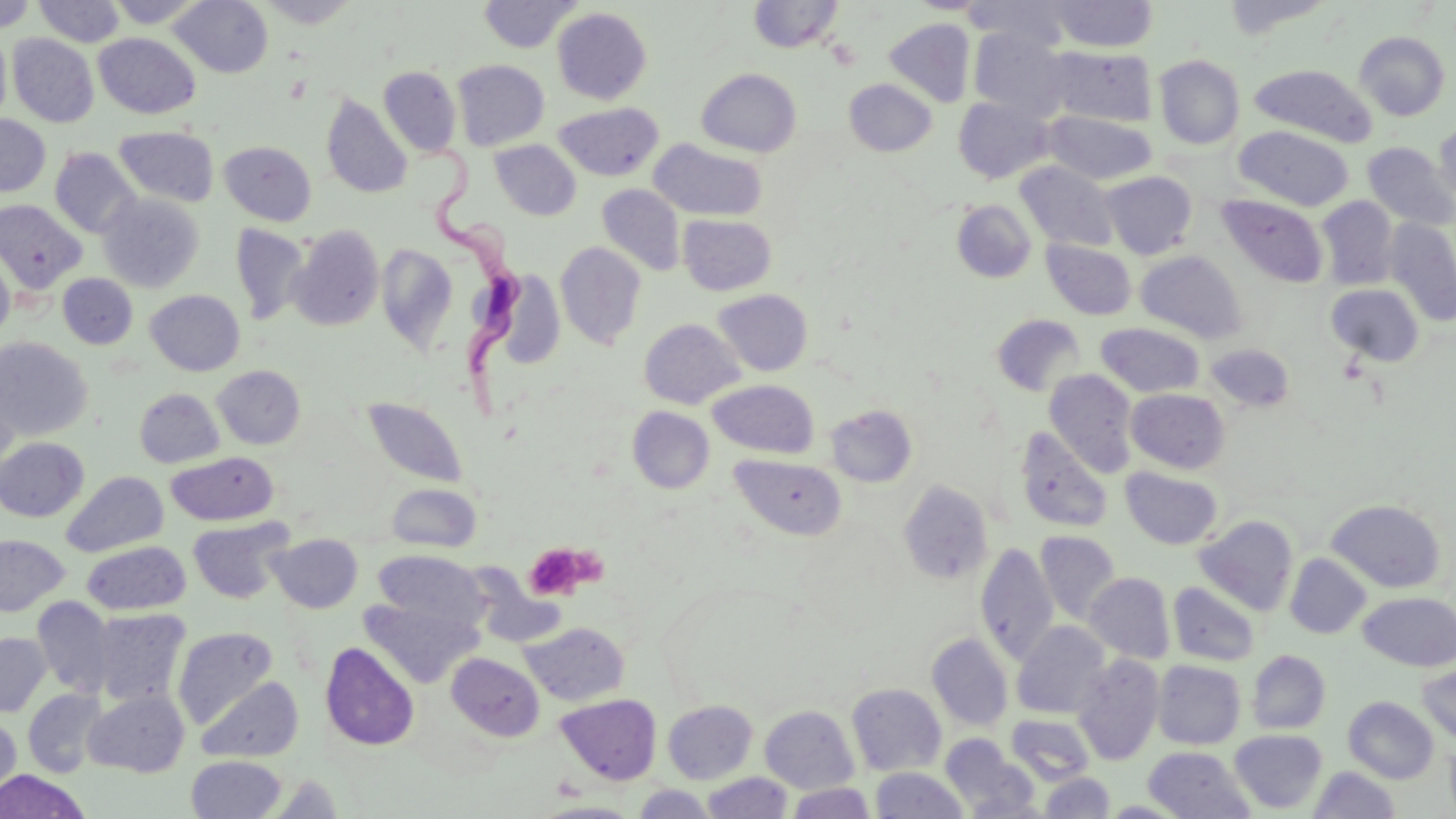
Approximate bounding boxes as (x1,y1)-(x2,y2) corner pairs in pixels. Uninfected red blood cell locations: (0,0)-(37,32), (34,0)-(125,46), (105,0)-(208,28), (169,0)-(273,77), (257,0)-(361,27), (477,0)-(582,53), (748,0)-(844,53), (911,0)-(989,14), (962,0)-(1074,52), (1220,0)-(1338,39), (1048,1)-(1159,52), (552,7)-(652,105), (884,19)-(975,107), (968,28)-(1072,120), (0,31)-(10,131), (1355,31)-(1450,121), (7,33)-(98,127), (94,33)-(200,119), (1046,46)-(1157,127), (1154,55)-(1245,150), (452,60)-(550,150), (1249,63)-(1378,147), (378,66)-(462,157), (696,68)-(802,157), (844,78)-(937,156), (321,93)-(413,199), (953,96)-(1055,183), (554,102)-(663,182), (1044,111)-(1157,185), (0,115)-(50,197), (1434,120)-(1456,206), (1234,125)-(1354,211), (115,126)-(219,207), (650,139)-(767,221), (490,140)-(581,220), (219,141)-(317,226), (1362,142)-(1455,229), (49,148)-(140,238), (1015,161)-(1118,252), (1100,171)-(1197,258), (597,184)-(686,276), (98,192)-(204,292), (1216,194)-(1328,288), (1316,196)-(1399,290), (951,199)-(1037,283), (0,200)-(86,294), (678,214)-(777,295), (1384,219)-(1456,325), (229,223)-(310,325), (287,224)-(385,331), (1041,239)-(1137,320), (555,241)-(646,350), (376,244)-(457,352), (0,247)-(15,343), (1135,250)-(1247,343), (497,270)-(566,367), (58,273)-(138,349), (1326,283)-(1425,366), (145,289)-(245,376), (712,289)-(813,376), (991,314)-(1085,397), (639,318)-(745,409), (1095,322)-(1205,398), (0,338)-(94,440), (1205,342)-(1295,413), (1,359)-(22,470), (212,365)-(306,449), (1044,368)-(1139,476), (708,379)-(819,458), (135,388)-(224,468), (1125,388)-(1230,474), (363,397)-(468,488), (826,404)-(918,488), (627,406)-(714,493), (1014,425)-(1114,534), (0,438)-(88,521), (166,451)-(278,525), (730,453)-(846,541), (1120,467)-(1223,550), (61,471)-(168,557), (897,480)-(994,585), (386,483)-(481,553), (1325,498)-(1447,593), (1194,515)-(1298,616), (187,517)-(292,604), (1036,530)-(1121,625), (267,533)-(363,613), (0,534)-(69,616), (82,541)-(190,615), (976,542)-(1058,665), (373,550)-(489,633), (1285,553)-(1371,639), (1084,572)-(1175,664), (1167,582)-(1261,667), (1358,591)-(1456,671), (360,596)-(479,688), (32,597)-(115,698), (91,608)-(191,709), (1012,621)-(1111,720), (520,622)-(629,706), (172,626)-(278,728), (0,632)-(51,717), (927,632)-(1014,731), (320,642)-(420,750), (1247,650)-(1331,734), (447,653)-(545,741), (1072,653)-(1164,765), (1153,660)-(1246,749), (1416,662)-(1456,744), (196,676)-(303,762), (847,683)-(946,776), (21,689)-(108,777), (84,690)-(190,777), (555,694)-(662,785), (1343,696)-(1439,783), (662,700)-(758,783), (760,705)-(860,793), (1005,713)-(1096,787), (0,714)-(21,799), (1230,729)-(1328,813), (941,734)-(1036,816), (1143,746)-(1254,818), (186,755)-(287,819), (1308,766)-(1401,818), (871,767)-(968,818), (0,770)-(90,819), (1040,772)-(1115,818), (702,773)-(793,819), (260,774)-(348,817), (786,782)-(875,818), (633,785)-(717,818). Platelet locations: (524,544)-(588,600). Trypanosoma brucei locations: (417,139)-(534,422). Slide-level diagnosis: Trypanosoma brucei. May-Grünwald-Giemsa stain. Image is 1456×819 pixels. Optical microscopy. One field of a larger specimen. Thin blood film. 1000x magnification.